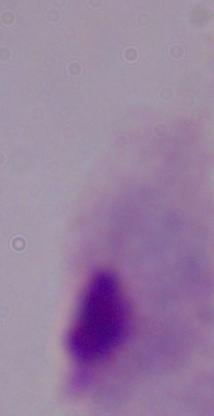
identification = trichomonad
modality = photomicrograph
magnification = 1000x